Comment on the morphology of the erythrocytes.
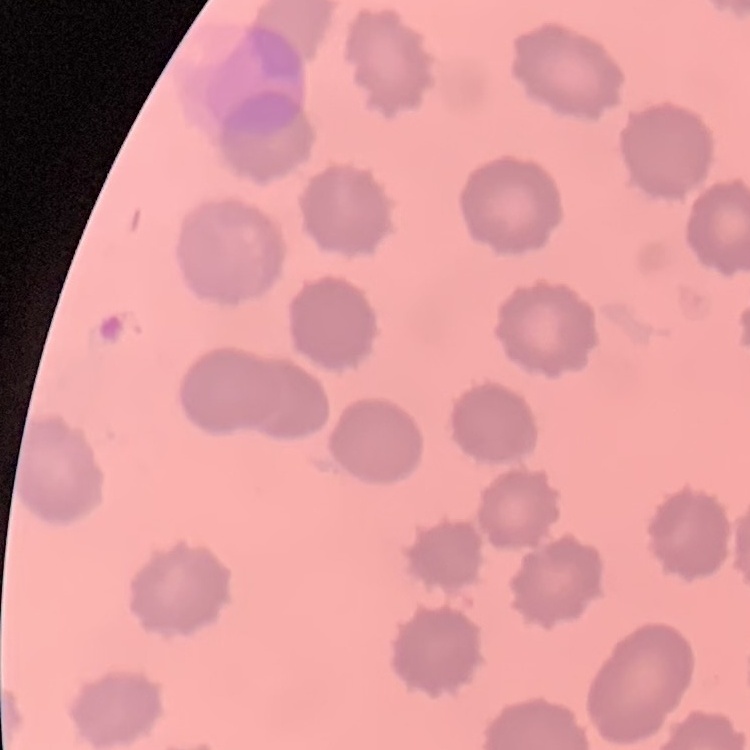
They show no rouleaux formation.

Summary:
  - Image type: square crop of a larger photomicrograph
  - Stain: Field's or Giemsa
  - Preparation: thin blood film